Name the parasite shown.
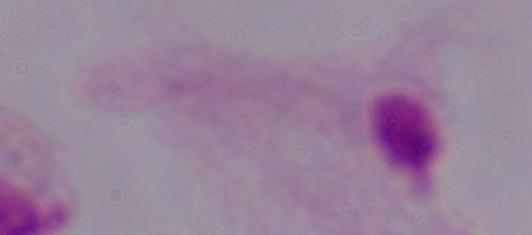

A trichomonad.

Summary:
  - Magnification: 1000x
  - Modality: photomicrograph